Locate every blood parasite and identify its species.
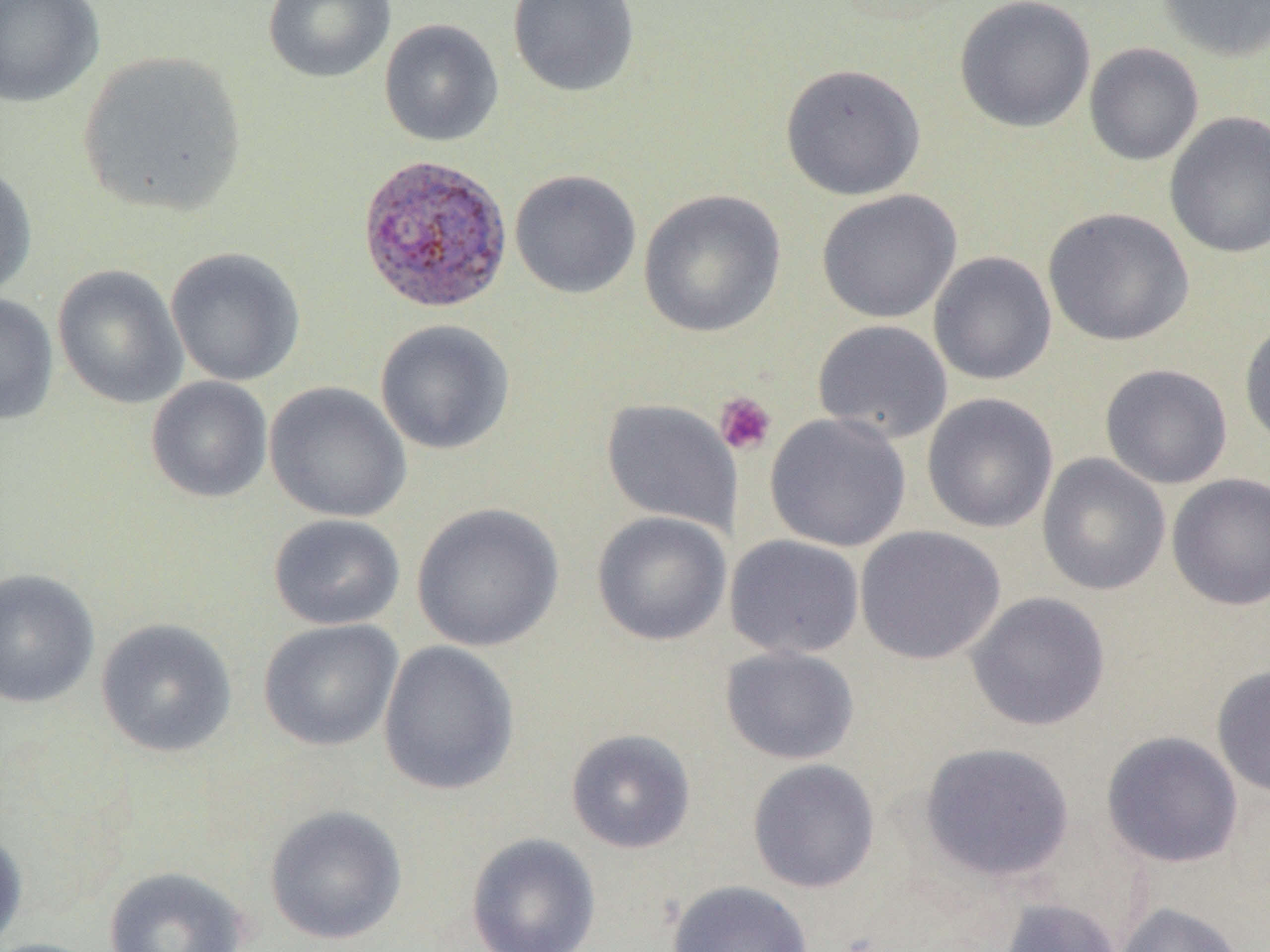

Approximate bounding boxes as (x1, y1, x2, y2) in pixels.
Plasmodium vivax-infected red blood cells: (356, 154, 513, 315).
No Plasmodium falciparum, Plasmodium ovale, Plasmodium malariae, Babesia divergens, or Trypanosoma brucei observed.

Uninfected red blood cell locations: (0, 0, 105, 108), (262, 0, 396, 84), (507, 0, 640, 98), (954, 0, 1095, 133), (1156, 0, 1270, 62), (379, 19, 504, 147), (1083, 42, 1204, 166), (78, 50, 248, 219), (780, 63, 926, 200), (1165, 111, 1270, 260), (0, 162, 37, 299), (509, 169, 642, 299), (637, 188, 786, 338), (816, 189, 962, 323), (1042, 207, 1194, 347), (165, 247, 306, 387), (928, 251, 1057, 386), (52, 264, 188, 409), (0, 293, 59, 426), (375, 319, 515, 455), (812, 319, 953, 444), (1238, 319, 1270, 451), (1099, 364, 1233, 489), (146, 376, 273, 503), (264, 381, 412, 523), (921, 392, 1058, 533), (601, 398, 742, 534), (765, 412, 911, 552), (1036, 453, 1171, 596), (1165, 473, 1270, 611), (411, 502, 564, 652), (592, 511, 732, 646), (268, 514, 405, 631), (855, 525, 1005, 665), (724, 534, 865, 659), (0, 568, 100, 709), (965, 591, 1111, 731), (95, 618, 237, 758), (258, 618, 403, 752), (378, 640, 519, 796), (720, 645, 860, 764), (1211, 663, 1270, 799), (566, 728, 696, 854), (1100, 730, 1244, 869), (919, 741, 1075, 883), (747, 758, 881, 893), (264, 804, 408, 945), (0, 827, 28, 948), (465, 832, 601, 952), (102, 865, 250, 952), (666, 879, 813, 952), (997, 896, 1123, 952), (1114, 901, 1247, 952), (0, 937, 103, 952). Platelet locations: (714, 391, 777, 456). Slide-level diagnosis: Plasmodium vivax. Optical microscopy. Single field of view. 1000x magnification. Thin blood smear. Image is 1270×952 pixels.